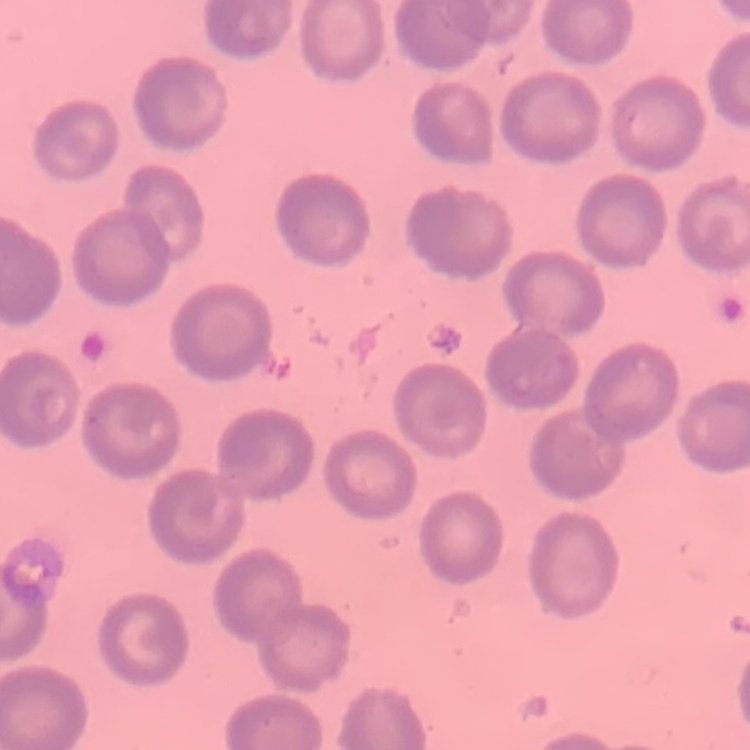
The erythrocytes show no rouleaux formation. Thin peripheral smear. One tile cut from a larger photomicrograph. Field's or Giemsa stain.